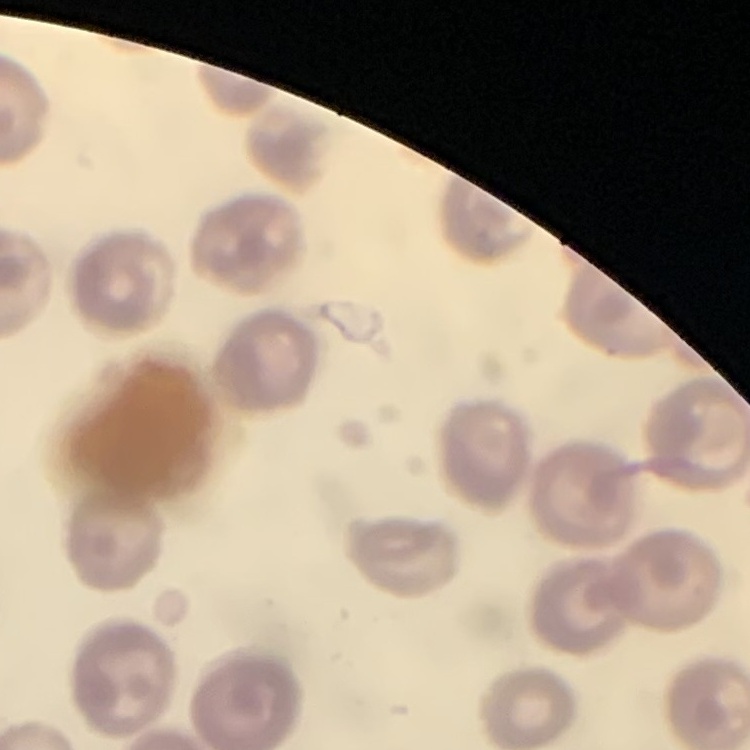

red blood cell morphology = no rouleaux formation
preparation = thin peripheral smear
image type = square crop of a larger photomicrograph
stain = Field's or Giemsa